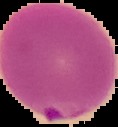
Summary:
  - Image type: cell region segmented out of the field of view; surrounding area masked to black
  - Preparation: thin blood film
  - Image size: 118×127 pixels
  - Malaria status: parasitized